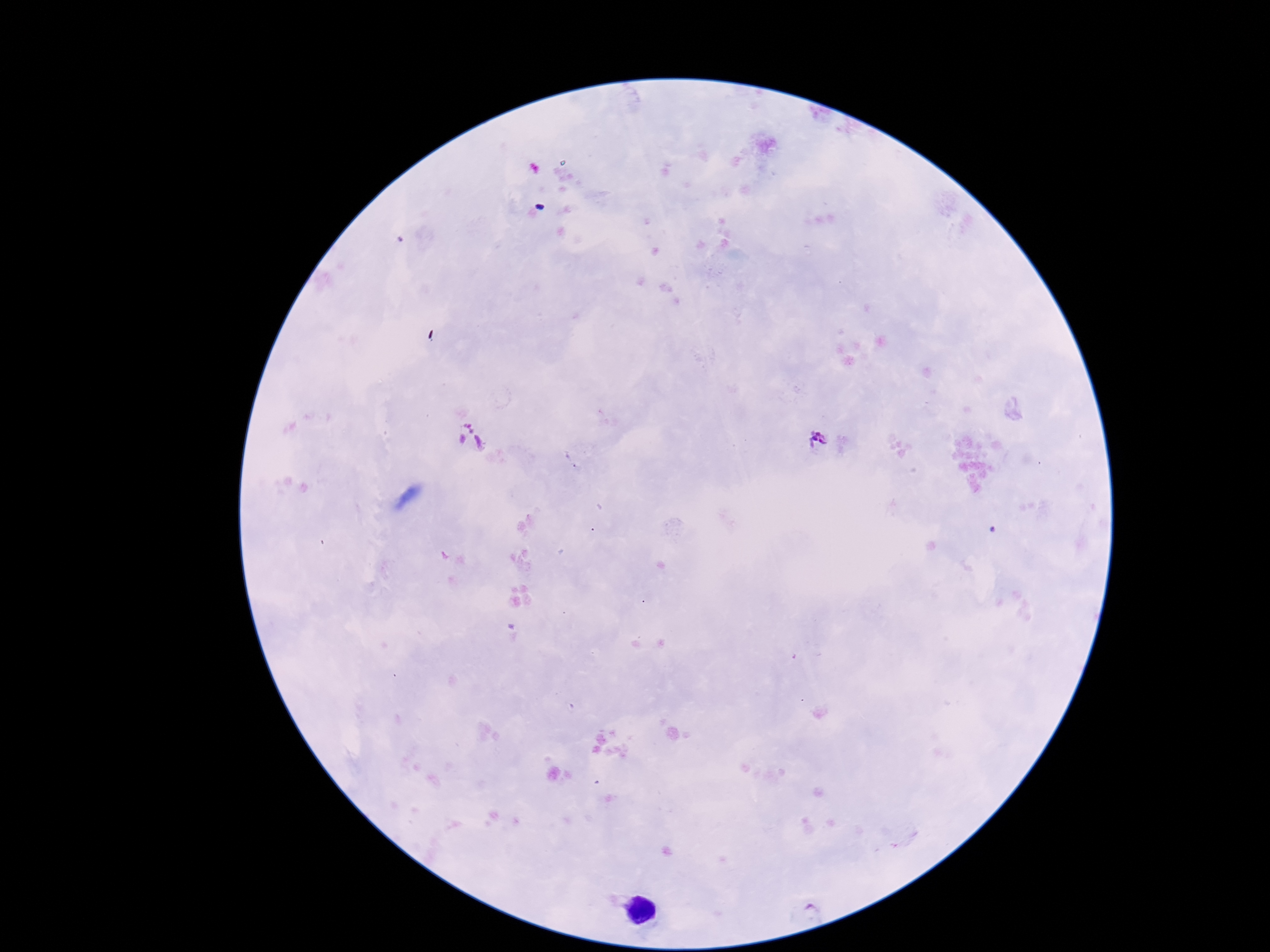

Approximate centers as {x, y} in pixels. Plasmodium parasite locations: {470, 437}, {818, 440}. Patient malaria status: positive. Thick blood smear. 100x magnification. Image is 1270×952 pixels. Giemsa-stained preparation. Smartphone photograph taken through the microscope eyepiece. Single field of view.